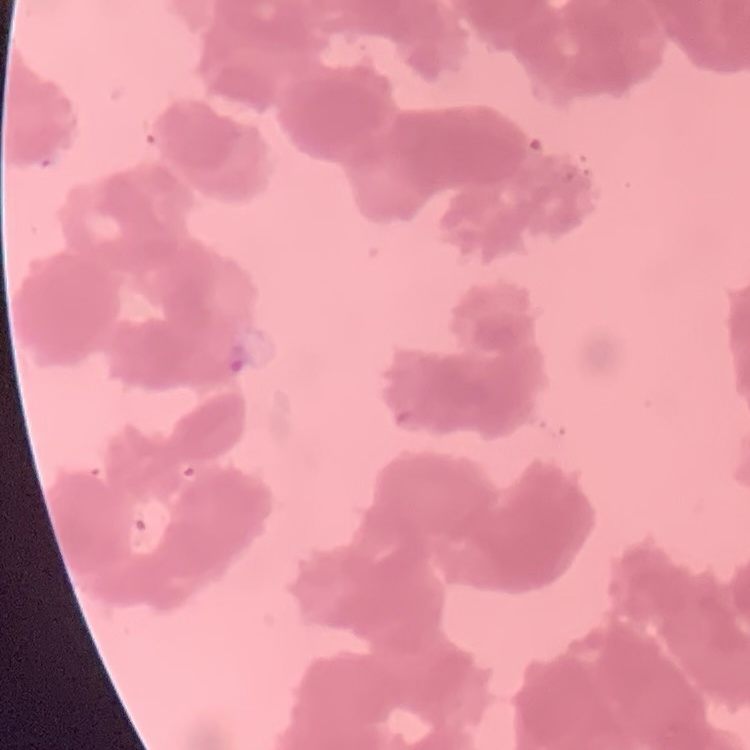

Summary:
  - Erythrocyte morphology: rouleaux formation
  - Preparation: thin blood film
  - Image type: one tile cut from a larger photomicrograph
  - Stain: Field's or Giemsa